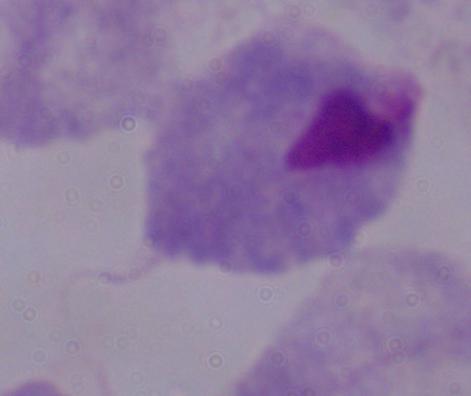
Summary:
  - Identification: trichomonad
  - Modality: micrograph
  - Magnification: 1000x